Outline platelets.
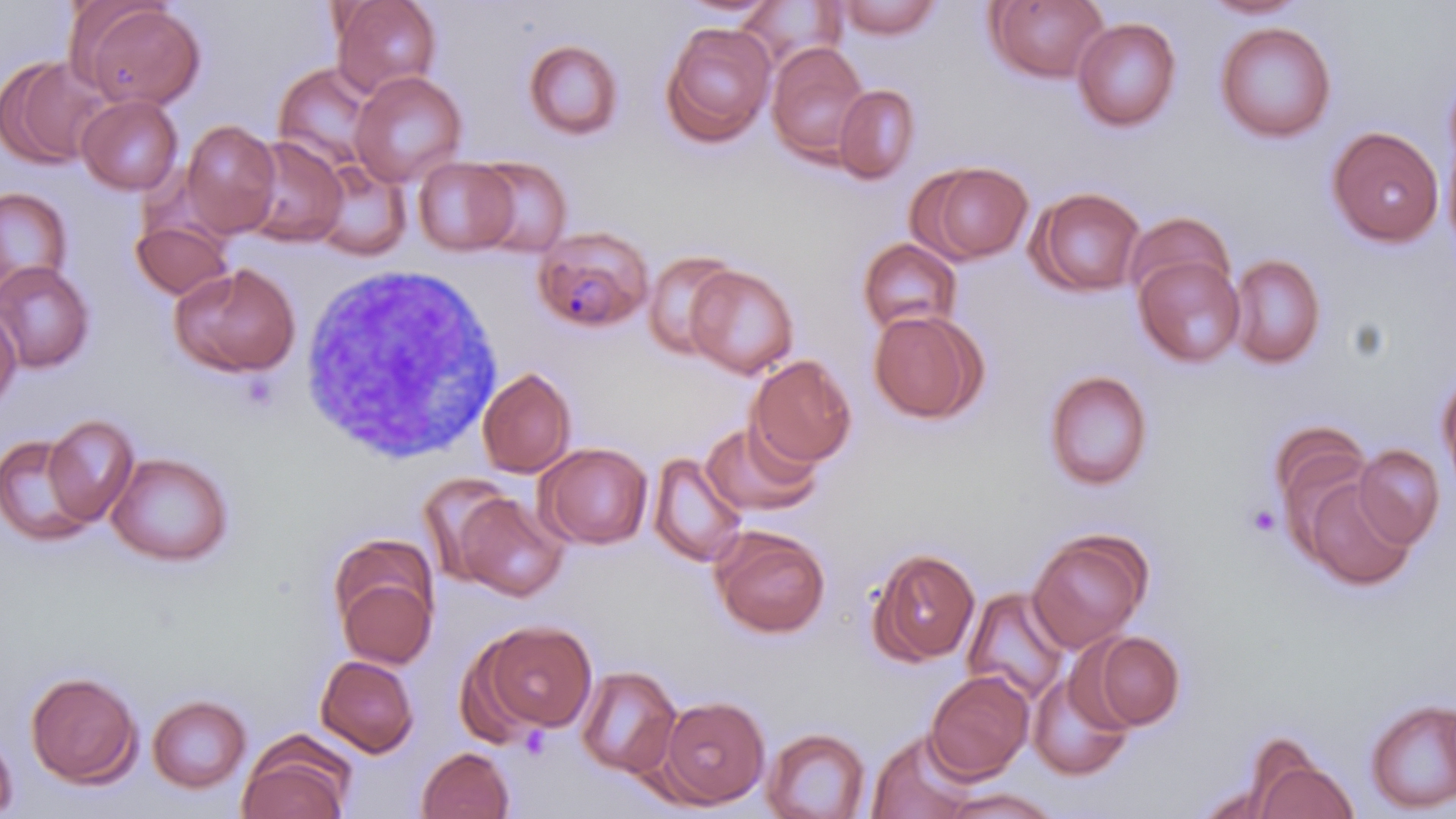

Approximate bounding boxes as named x1/y1/x2/y2 corners in pixels.
Platelets: (x1=1243, y1=502, x2=1282, y2=539).

Uninfected red blood cell locations: (x1=331, y1=0, x2=442, y2=97), (x1=671, y1=0, x2=783, y2=20), (x1=985, y1=0, x2=1110, y2=84), (x1=1198, y1=0, x2=1309, y2=20), (x1=735, y1=1, x2=846, y2=73), (x1=834, y1=1, x2=943, y2=39), (x1=74, y1=2, x2=206, y2=111), (x1=1072, y1=17, x2=1181, y2=132), (x1=660, y1=21, x2=777, y2=147), (x1=1214, y1=21, x2=1336, y2=143), (x1=523, y1=40, x2=624, y2=141), (x1=766, y1=42, x2=870, y2=164), (x1=1, y1=55, x2=109, y2=170), (x1=273, y1=62, x2=382, y2=173), (x1=350, y1=71, x2=467, y2=187), (x1=834, y1=84, x2=920, y2=184), (x1=77, y1=94, x2=183, y2=195), (x1=181, y1=119, x2=281, y2=237), (x1=1326, y1=125, x2=1445, y2=248), (x1=1441, y1=131, x2=1456, y2=261), (x1=242, y1=136, x2=348, y2=248), (x1=469, y1=156, x2=572, y2=257), (x1=413, y1=157, x2=519, y2=256), (x1=310, y1=160, x2=412, y2=261), (x1=917, y1=161, x2=1033, y2=263), (x1=0, y1=187, x2=72, y2=297), (x1=1027, y1=187, x2=1146, y2=298), (x1=1124, y1=211, x2=1237, y2=309), (x1=130, y1=219, x2=233, y2=300), (x1=857, y1=238, x2=962, y2=336), (x1=642, y1=250, x2=742, y2=360), (x1=1132, y1=253, x2=1246, y2=368), (x1=1228, y1=254, x2=1326, y2=370), (x1=0, y1=261, x2=95, y2=373), (x1=170, y1=262, x2=302, y2=378), (x1=686, y1=265, x2=799, y2=378), (x1=0, y1=305, x2=21, y2=413), (x1=867, y1=309, x2=988, y2=425), (x1=748, y1=355, x2=858, y2=468), (x1=477, y1=367, x2=576, y2=478), (x1=1043, y1=369, x2=1154, y2=492), (x1=1437, y1=370, x2=1456, y2=496), (x1=43, y1=415, x2=139, y2=526), (x1=700, y1=419, x2=822, y2=518), (x1=1268, y1=420, x2=1371, y2=528), (x1=0, y1=432, x2=100, y2=545), (x1=536, y1=443, x2=653, y2=549), (x1=1353, y1=445, x2=1445, y2=549), (x1=106, y1=451, x2=234, y2=566), (x1=646, y1=451, x2=749, y2=569), (x1=419, y1=472, x2=519, y2=585), (x1=1303, y1=477, x2=1417, y2=590), (x1=452, y1=492, x2=569, y2=601), (x1=711, y1=526, x2=831, y2=638), (x1=1027, y1=527, x2=1152, y2=652), (x1=330, y1=546, x2=439, y2=669), (x1=867, y1=548, x2=980, y2=666), (x1=962, y1=587, x2=1071, y2=703), (x1=472, y1=619, x2=599, y2=735), (x1=1086, y1=630, x2=1185, y2=731), (x1=315, y1=654, x2=420, y2=757), (x1=575, y1=665, x2=682, y2=778), (x1=1027, y1=668, x2=1135, y2=781), (x1=25, y1=670, x2=142, y2=788), (x1=925, y1=670, x2=1035, y2=781), (x1=147, y1=694, x2=252, y2=793), (x1=657, y1=696, x2=770, y2=809), (x1=1364, y1=698, x2=1456, y2=813), (x1=0, y1=724, x2=17, y2=816), (x1=761, y1=727, x2=871, y2=818), (x1=867, y1=729, x2=980, y2=819), (x1=237, y1=737, x2=355, y2=819), (x1=416, y1=747, x2=515, y2=819), (x1=1248, y1=751, x2=1358, y2=819), (x1=941, y1=787, x2=1060, y2=818). Plasmodium malariae-infected red blood cell locations: (x1=532, y1=227, x2=654, y2=334). White blood cell locations: (x1=297, y1=261, x2=504, y2=464). Slide-level diagnosis: Plasmodium malariae. Optical microscopy. One field of a larger specimen. Captured at 1000x magnification. Thin blood film. Image is 1456×819 pixels. May-Grünwald-Giemsa-stained preparation.